Locate the red blood cells and classify each one as Plasmodium falciparum-infected, uninfected, or of indeterminate infection status.
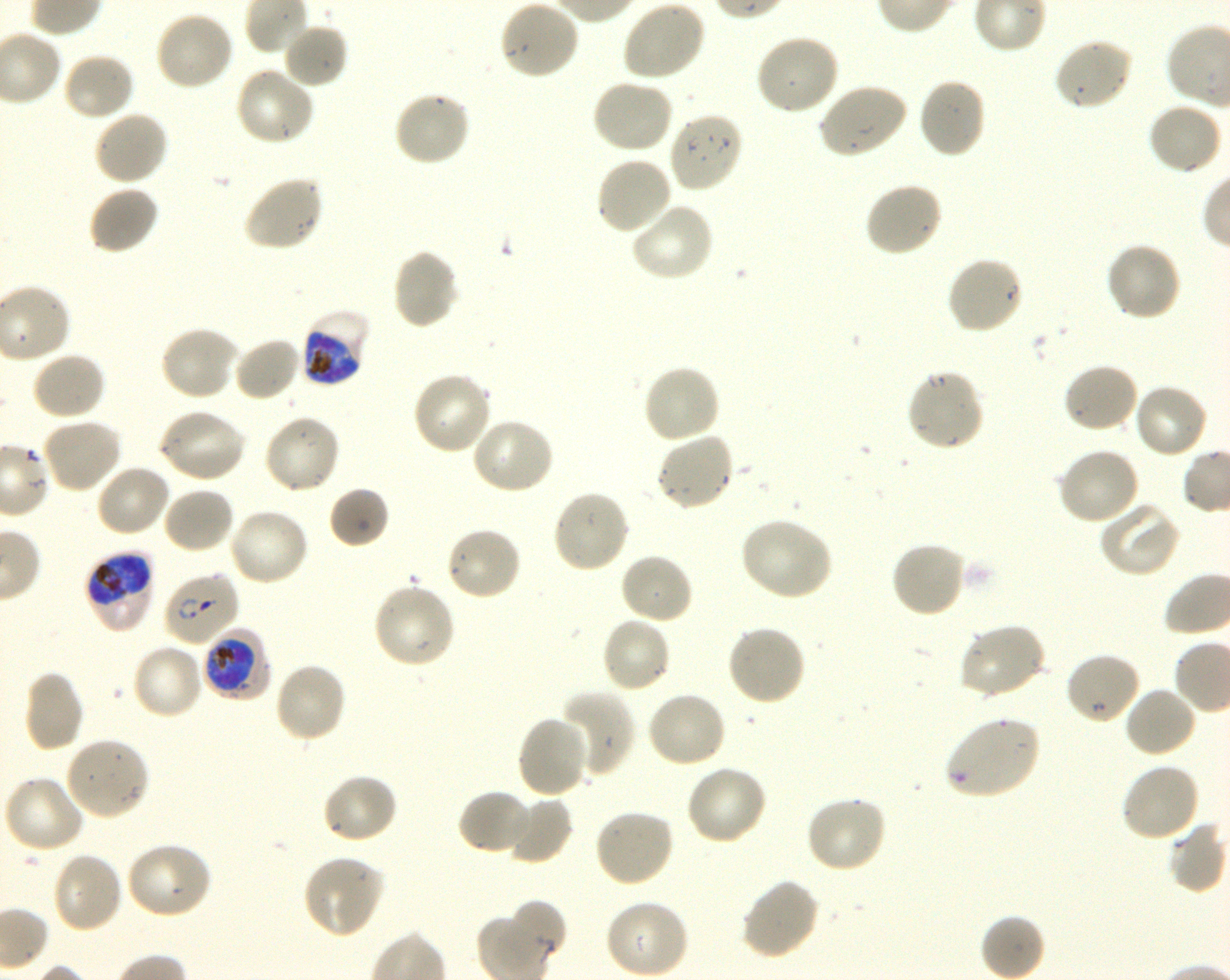
Approximate bounding rectangles given as corner coordinates in pixels from the top-left. Not every red blood cell is marked. A life-cycle stage — or a range of stages, where the recorded stages span more than one — follows each staged infected red blood cell.
Infected red blood cells: (x1=300, y1=308, x2=372, y2=388) early trophozoite to late schizont; (x1=84, y1=553, x2=156, y2=631) early trophozoite to early schizont; (x1=163, y1=572, x2=240, y2=647) ring; (x1=201, y1=627, x2=272, y2=700) trophozoite.
Uninfected red blood cells: (x1=499, y1=0, x2=581, y2=81), (x1=621, y1=0, x2=706, y2=82), (x1=153, y1=10, x2=234, y2=92), (x1=282, y1=21, x2=349, y2=89), (x1=754, y1=32, x2=840, y2=116), (x1=1052, y1=35, x2=1134, y2=112), (x1=61, y1=51, x2=136, y2=121), (x1=235, y1=66, x2=316, y2=147), (x1=590, y1=77, x2=674, y2=154), (x1=917, y1=78, x2=987, y2=160), (x1=817, y1=82, x2=908, y2=160), (x1=392, y1=90, x2=472, y2=167), (x1=1147, y1=102, x2=1223, y2=177), (x1=92, y1=110, x2=169, y2=186), (x1=667, y1=111, x2=744, y2=194), (x1=594, y1=155, x2=673, y2=237), (x1=242, y1=173, x2=324, y2=253), (x1=864, y1=181, x2=944, y2=258), (x1=87, y1=185, x2=160, y2=255), (x1=628, y1=201, x2=715, y2=282), (x1=1104, y1=241, x2=1182, y2=322), (x1=391, y1=248, x2=460, y2=331), (x1=945, y1=255, x2=1024, y2=335), (x1=159, y1=326, x2=240, y2=402), (x1=232, y1=336, x2=303, y2=403), (x1=30, y1=351, x2=106, y2=422), (x1=1062, y1=362, x2=1140, y2=434), (x1=640, y1=363, x2=721, y2=445), (x1=905, y1=368, x2=986, y2=453), (x1=411, y1=371, x2=494, y2=456), (x1=1133, y1=382, x2=1210, y2=460), (x1=156, y1=407, x2=247, y2=484), (x1=262, y1=414, x2=341, y2=496), (x1=39, y1=415, x2=123, y2=494), (x1=470, y1=417, x2=556, y2=494), (x1=655, y1=432, x2=736, y2=513), (x1=1056, y1=446, x2=1142, y2=526), (x1=95, y1=463, x2=173, y2=539), (x1=162, y1=486, x2=236, y2=554), (x1=329, y1=486, x2=390, y2=549), (x1=551, y1=489, x2=631, y2=574), (x1=1098, y1=500, x2=1181, y2=578), (x1=227, y1=507, x2=311, y2=587), (x1=739, y1=517, x2=834, y2=601), (x1=444, y1=525, x2=523, y2=602), (x1=890, y1=540, x2=966, y2=619), (x1=619, y1=552, x2=694, y2=626), (x1=371, y1=581, x2=457, y2=670), (x1=600, y1=616, x2=672, y2=694), (x1=957, y1=622, x2=1047, y2=700), (x1=725, y1=624, x2=807, y2=707), (x1=131, y1=642, x2=205, y2=720), (x1=1064, y1=651, x2=1141, y2=726), (x1=272, y1=660, x2=347, y2=744), (x1=22, y1=671, x2=86, y2=752), (x1=1124, y1=685, x2=1199, y2=758), (x1=555, y1=690, x2=635, y2=778), (x1=645, y1=691, x2=728, y2=769), (x1=516, y1=714, x2=593, y2=798), (x1=943, y1=716, x2=1040, y2=800), (x1=64, y1=735, x2=150, y2=821), (x1=1120, y1=761, x2=1201, y2=844), (x1=684, y1=765, x2=769, y2=847), (x1=321, y1=773, x2=398, y2=845), (x1=1, y1=775, x2=85, y2=855), (x1=457, y1=788, x2=533, y2=856), (x1=505, y1=796, x2=573, y2=865), (x1=804, y1=796, x2=889, y2=874), (x1=593, y1=807, x2=675, y2=887), (x1=1167, y1=820, x2=1227, y2=893), (x1=125, y1=841, x2=214, y2=921), (x1=50, y1=851, x2=124, y2=934), (x1=301, y1=853, x2=386, y2=938), (x1=739, y1=877, x2=820, y2=961), (x1=603, y1=898, x2=690, y2=978), (x1=508, y1=900, x2=567, y2=961).
No red blood cells of indeterminate infection status observed.

Shaking in-vitro culture of Plasmodium falciparum strain 3D7. Life-cycle stages observed: ring, trophozoite. Giemsa stain. 100x oil-immersion objective, numerical aperture 1.30. Thin blood film. Image is 1230×980 pixels. Blood group of the donor: O+. Single field of view.